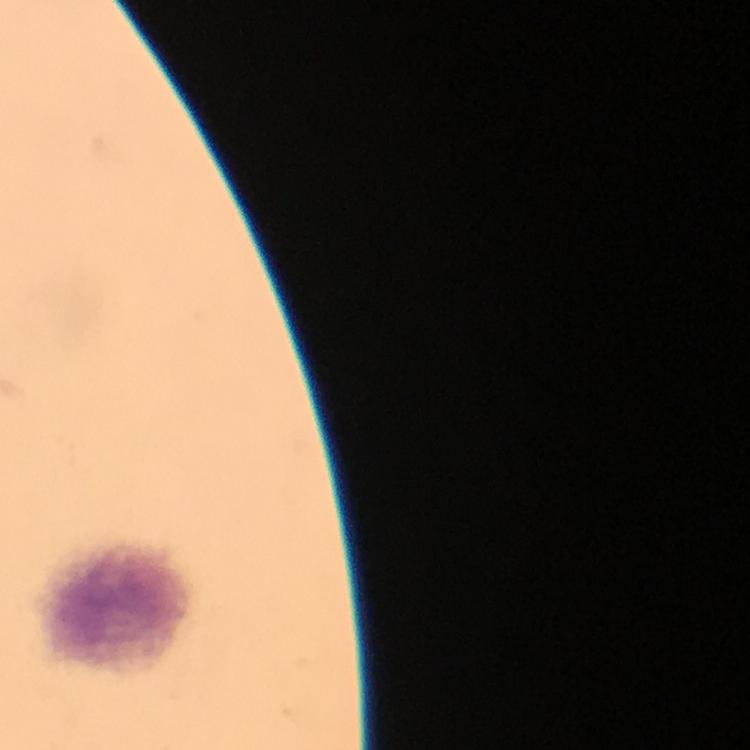

Approximate centers as [x, y] in pixels. Leukocyte locations: [120, 608]. Image is 750×750 pixels. From a diagnostic examination for malaria. Thick smear. 100x magnification. Plasmodium parasites: none seen. Giemsa stain. Photographed through the microscope with a smartphone camera. Cropped region of a single field of view. Immersion oil applied.